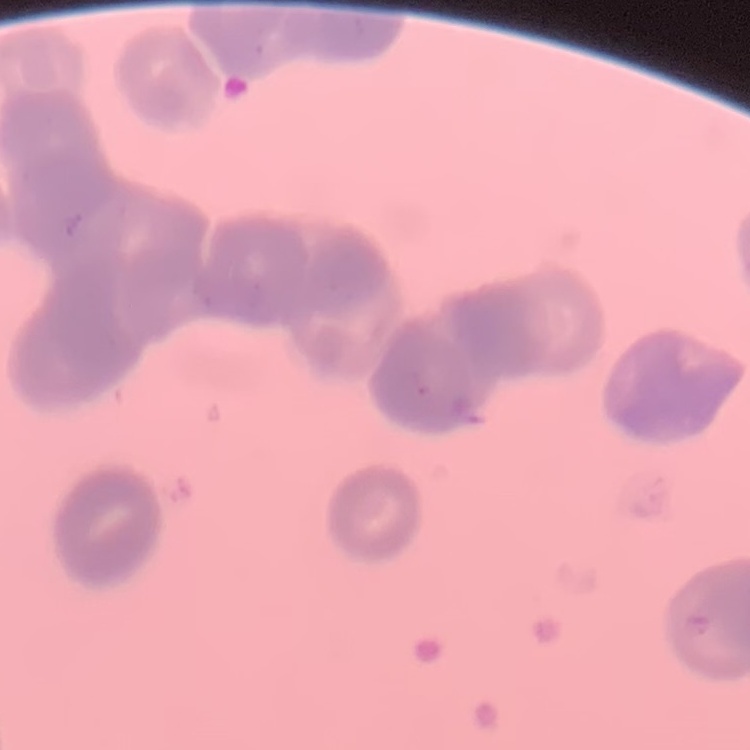 The erythrocytes exhibit rouleaux formation. Field's or Giemsa stain. Thin blood smear. One tile cut from a larger photomicrograph.